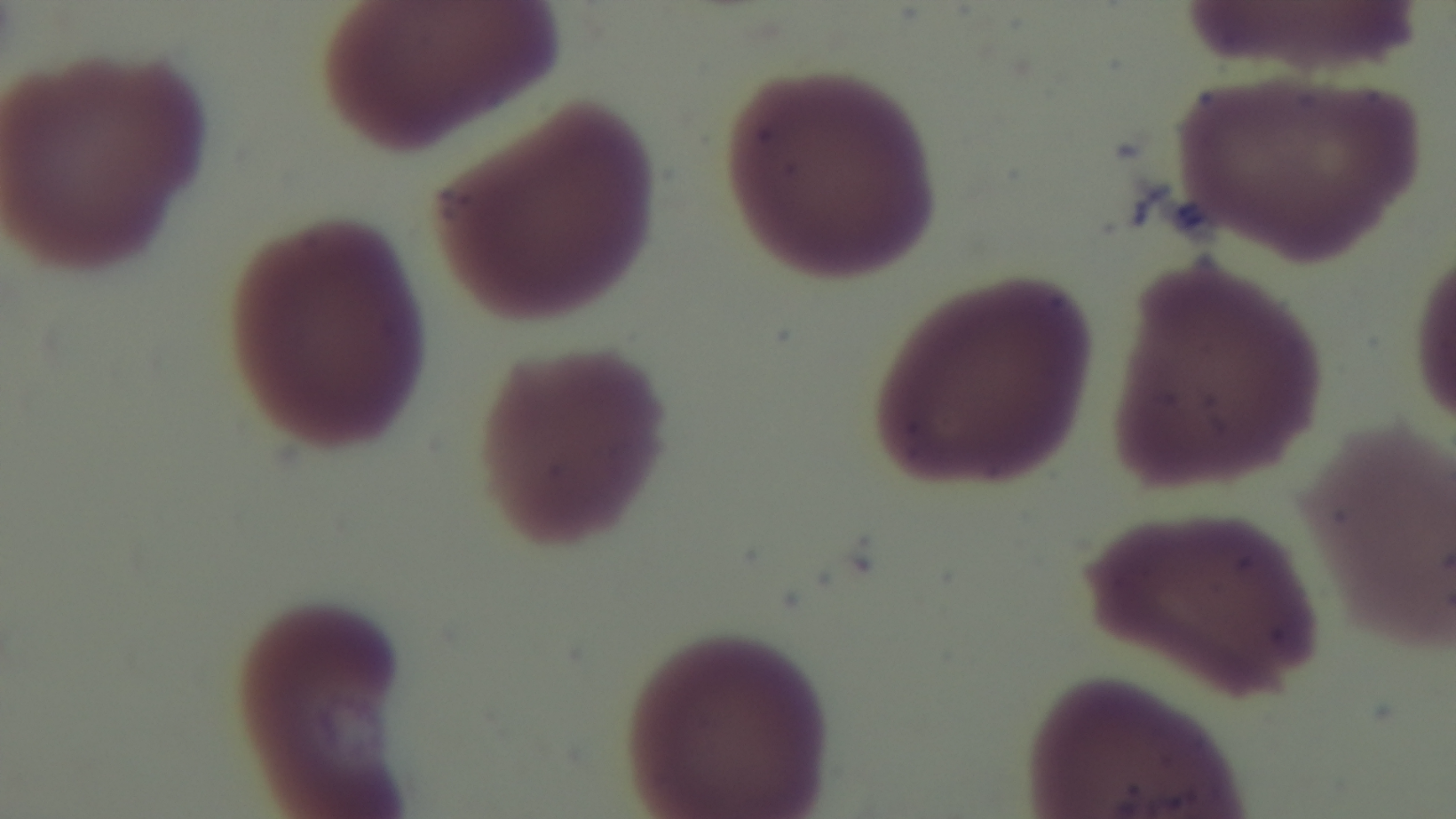
Summary:
  - Stain: Giemsa
  - Preparation: thin smear
  - Malaria status: negative
  - Modality: light microscopy
  - Field of view: single
  - Objective: 100x oil immersion
  - Capture: mounted 4K digital camera